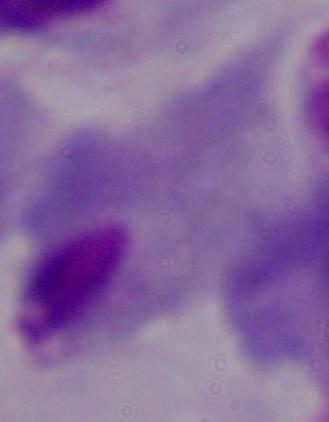
Summary:
  - Identification: trichomonad
  - Magnification: 1000x
  - Modality: micrograph